Classify this cell by malaria status.
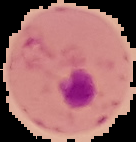
It is parasitized.

image type = segmented cell region on a black background
preparation = thin blood film
image size = 136×142 pixels